Give the extent of all Plasmodium falciparum-infected red blood cells.
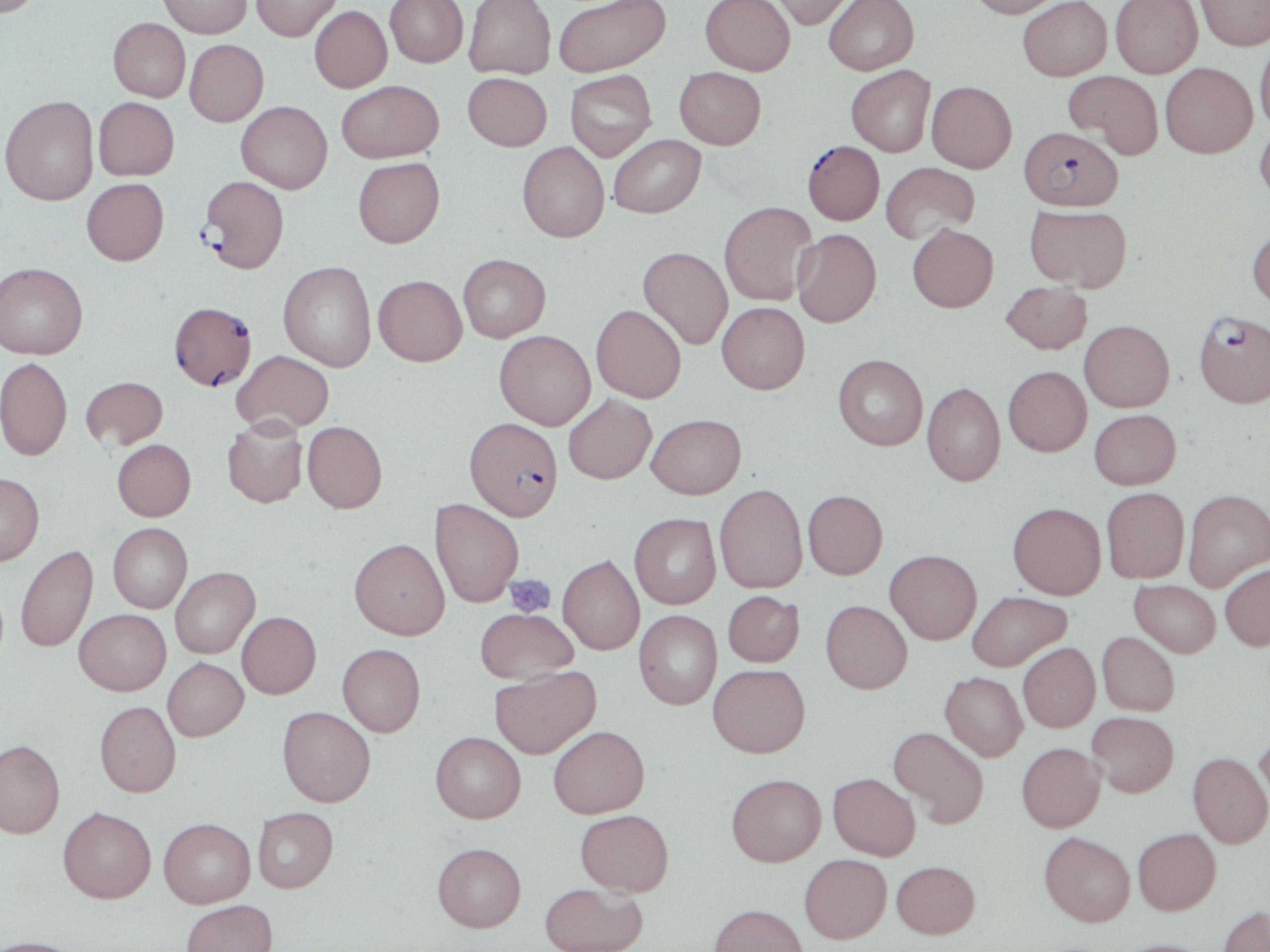
Approximate bounding boxes as (x1, y1, x2, y2) in pixels.
Plasmodium falciparum-infected red blood cells: (1020, 126, 1123, 211), (806, 143, 888, 227), (198, 176, 289, 274), (169, 301, 256, 390), (1193, 310, 1270, 408), (465, 417, 562, 520).

slide-level diagnosis = Plasmodium falciparum
modality = light microscopy
preparation = thin blood film
magnification = 1000x
platelet locations = approximate bounding boxes as (x1, y1, x2, y2) in pixels: (504, 573, 556, 617)
stain = May-Grünwald-Giemsa
uninfected red blood cell locations = approximate bounding boxes as (x1, y1, x2, y2) in pixels: (0, 0, 45, 17), (159, 0, 252, 38), (250, 0, 342, 41), (384, 0, 468, 67), (464, 0, 556, 79), (553, 0, 670, 76), (700, 0, 795, 75), (768, 0, 856, 30), (824, 0, 918, 75), (967, 0, 1064, 18), (1018, 0, 1112, 81), (1110, 0, 1202, 77), (1196, 0, 1270, 51), (310, 5, 392, 92), (108, 17, 191, 102), (1254, 36, 1270, 134), (184, 39, 268, 126), (1160, 62, 1257, 157), (846, 65, 935, 156), (674, 67, 765, 149), (565, 70, 657, 161), (1064, 70, 1163, 158), (463, 72, 552, 150), (336, 80, 443, 163), (926, 81, 1017, 172), (1, 95, 99, 205), (93, 97, 179, 180), (236, 101, 333, 193), (1255, 122, 1270, 206), (608, 134, 706, 218), (517, 142, 609, 242), (353, 156, 445, 248), (881, 162, 979, 244), (81, 178, 169, 265), (719, 201, 817, 305), (1025, 203, 1132, 291), (907, 223, 998, 312), (1247, 225, 1270, 311), (792, 229, 881, 327), (638, 246, 733, 350), (458, 254, 550, 342), (278, 261, 376, 372), (0, 262, 88, 359), (373, 275, 467, 366), (1001, 280, 1092, 353), (717, 301, 810, 394), (591, 304, 686, 402), (1079, 320, 1174, 411), (494, 330, 595, 430), (232, 350, 334, 433), (833, 354, 927, 450), (0, 356, 73, 460), (1003, 365, 1091, 456), (80, 376, 168, 450), (922, 382, 1005, 486), (564, 394, 657, 484), (1089, 409, 1181, 489), (646, 413, 745, 498), (222, 417, 308, 508), (302, 421, 387, 512), (112, 439, 196, 521), (0, 473, 44, 565), (715, 483, 807, 593), (1101, 487, 1189, 583), (1183, 488, 1270, 592), (803, 490, 888, 579), (430, 499, 524, 607), (1007, 502, 1106, 599), (629, 513, 720, 609), (108, 523, 192, 613), (349, 538, 450, 639), (16, 544, 98, 653), (885, 549, 981, 644), (558, 555, 644, 654), (1220, 563, 1270, 651), (170, 567, 260, 658), (1129, 579, 1220, 657), (723, 590, 804, 667), (967, 590, 1072, 671), (821, 600, 912, 693), (74, 608, 170, 695), (475, 608, 578, 684), (634, 610, 722, 709), (237, 611, 321, 698), (1097, 631, 1180, 715), (1018, 642, 1100, 732), (337, 643, 425, 736), (162, 657, 248, 741), (708, 663, 810, 757), (489, 665, 600, 759), (940, 672, 1028, 761), (95, 701, 181, 797), (278, 706, 375, 806), (1087, 711, 1179, 796), (548, 725, 649, 818), (889, 726, 990, 828), (1254, 726, 1270, 817), (431, 731, 526, 822), (0, 739, 65, 838), (1016, 742, 1105, 832), (1187, 750, 1270, 848), (828, 772, 920, 860), (726, 773, 826, 866), (58, 806, 156, 903), (253, 806, 338, 892), (576, 809, 674, 896), (159, 818, 255, 908), (1133, 828, 1221, 915), (1039, 831, 1134, 926), (432, 842, 526, 931), (799, 853, 891, 942), (891, 860, 980, 939), (539, 883, 648, 952), (181, 900, 277, 952), (708, 903, 808, 952), (1218, 905, 1269, 952), (0, 936, 84, 952), (1112, 938, 1220, 952)
image size = 1270×952 pixels
field of view = one of a larger specimen